Identify the cell.
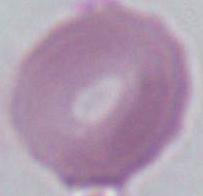

An erythrocyte.

Summary:
  - Magnification: 1000x
  - Modality: photomicrograph